Comment on the morphology of the red blood cells.
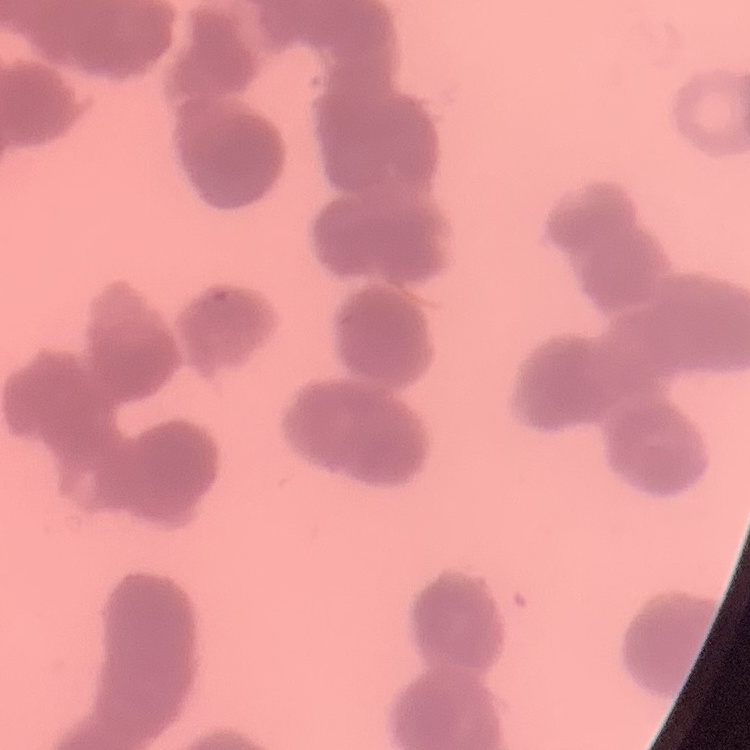

Rouleaux formation.

Stained with either Field's or Giemsa. Thin peripheral smear. One tile cut from a larger photomicrograph.